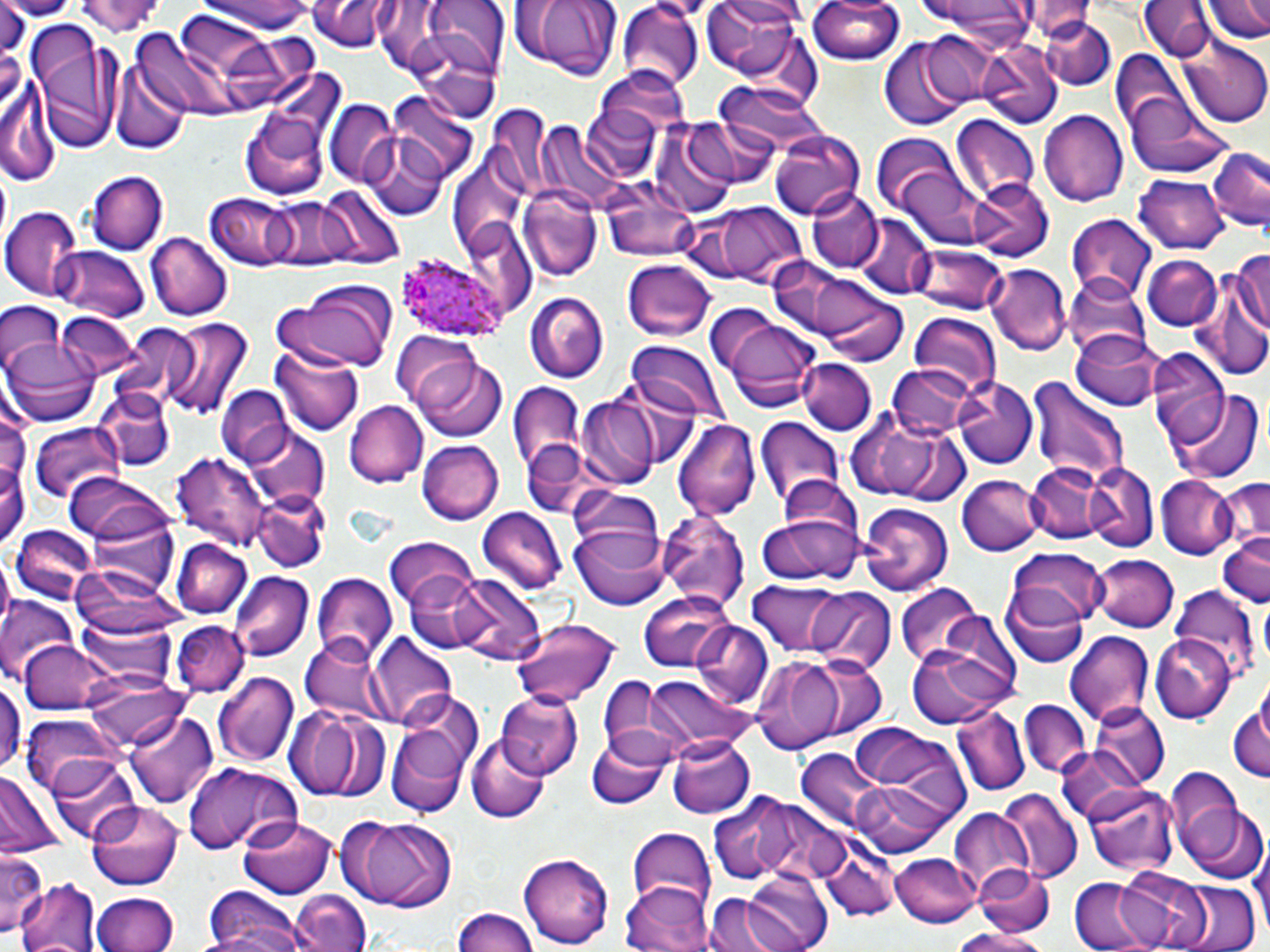 Approximate bounding boxes as named x1/y1/x2/y2 corners in pixels. Plasmodium ovale-infected red blood cell locations: (x1=397, y1=255, x2=504, y2=344). Uninfected red blood cell locations: (x1=76, y1=0, x2=167, y2=42), (x1=193, y1=0, x2=316, y2=35), (x1=310, y1=0, x2=395, y2=52), (x1=424, y1=0, x2=509, y2=77), (x1=507, y1=0, x2=624, y2=81), (x1=700, y1=0, x2=807, y2=88), (x1=804, y1=0, x2=908, y2=67), (x1=922, y1=0, x2=1037, y2=42), (x1=1202, y1=0, x2=1270, y2=43), (x1=1140, y1=1, x2=1212, y2=62), (x1=1018, y1=2, x2=1099, y2=43), (x1=618, y1=3, x2=704, y2=90), (x1=1, y1=7, x2=35, y2=54), (x1=1039, y1=16, x2=1115, y2=90), (x1=25, y1=21, x2=120, y2=151), (x1=403, y1=24, x2=504, y2=125), (x1=910, y1=29, x2=1002, y2=110), (x1=134, y1=31, x2=234, y2=117), (x1=220, y1=34, x2=332, y2=111), (x1=1180, y1=38, x2=1269, y2=127), (x1=879, y1=39, x2=974, y2=131), (x1=981, y1=42, x2=1061, y2=128), (x1=1110, y1=50, x2=1185, y2=132), (x1=109, y1=61, x2=188, y2=153), (x1=596, y1=67, x2=692, y2=144), (x1=715, y1=81, x2=828, y2=155), (x1=2, y1=87, x2=56, y2=187), (x1=238, y1=91, x2=335, y2=205), (x1=390, y1=94, x2=480, y2=184), (x1=1126, y1=94, x2=1235, y2=178), (x1=489, y1=96, x2=566, y2=197), (x1=325, y1=100, x2=398, y2=185), (x1=1039, y1=109, x2=1129, y2=207), (x1=680, y1=116, x2=793, y2=187), (x1=950, y1=116, x2=1038, y2=203), (x1=538, y1=124, x2=623, y2=211), (x1=649, y1=126, x2=738, y2=216), (x1=770, y1=130, x2=864, y2=218), (x1=361, y1=135, x2=450, y2=220), (x1=869, y1=135, x2=961, y2=212), (x1=1206, y1=145, x2=1269, y2=233), (x1=446, y1=150, x2=531, y2=254), (x1=886, y1=163, x2=992, y2=246), (x1=87, y1=171, x2=167, y2=255), (x1=1134, y1=172, x2=1227, y2=255), (x1=968, y1=178, x2=1052, y2=262), (x1=518, y1=187, x2=603, y2=283), (x1=314, y1=188, x2=404, y2=271), (x1=808, y1=189, x2=883, y2=274), (x1=208, y1=192, x2=303, y2=269), (x1=605, y1=192, x2=701, y2=263), (x1=266, y1=199, x2=347, y2=269), (x1=681, y1=201, x2=808, y2=287), (x1=1, y1=208, x2=83, y2=299), (x1=1066, y1=213, x2=1158, y2=303), (x1=855, y1=218, x2=936, y2=298), (x1=146, y1=230, x2=230, y2=319), (x1=910, y1=243, x2=1008, y2=315), (x1=1230, y1=244, x2=1270, y2=343), (x1=51, y1=245, x2=148, y2=323), (x1=1143, y1=255, x2=1222, y2=332), (x1=620, y1=259, x2=717, y2=341), (x1=770, y1=260, x2=890, y2=348), (x1=985, y1=264, x2=1071, y2=355), (x1=1190, y1=269, x2=1270, y2=384), (x1=1065, y1=280, x2=1147, y2=365), (x1=274, y1=287, x2=395, y2=372), (x1=818, y1=288, x2=908, y2=367), (x1=525, y1=291, x2=609, y2=384), (x1=0, y1=299, x2=65, y2=373), (x1=56, y1=312, x2=137, y2=380), (x1=907, y1=312, x2=1001, y2=394), (x1=716, y1=316, x2=822, y2=411), (x1=160, y1=318, x2=252, y2=422), (x1=116, y1=322, x2=209, y2=409), (x1=1072, y1=328, x2=1163, y2=410), (x1=393, y1=334, x2=483, y2=412), (x1=3, y1=339, x2=100, y2=427), (x1=629, y1=343, x2=722, y2=421), (x1=1148, y1=344, x2=1229, y2=446), (x1=270, y1=346, x2=367, y2=436), (x1=416, y1=357, x2=507, y2=443), (x1=796, y1=358, x2=878, y2=436), (x1=888, y1=364, x2=973, y2=440), (x1=598, y1=375, x2=706, y2=469), (x1=1026, y1=376, x2=1130, y2=488), (x1=952, y1=377, x2=1036, y2=470), (x1=508, y1=382, x2=586, y2=479), (x1=94, y1=385, x2=174, y2=468), (x1=218, y1=385, x2=290, y2=467), (x1=1172, y1=390, x2=1262, y2=481), (x1=577, y1=397, x2=660, y2=487), (x1=343, y1=400, x2=428, y2=487), (x1=843, y1=411, x2=971, y2=504), (x1=676, y1=418, x2=762, y2=520), (x1=754, y1=418, x2=842, y2=509), (x1=26, y1=423, x2=130, y2=510), (x1=240, y1=426, x2=331, y2=510), (x1=419, y1=440, x2=502, y2=525), (x1=522, y1=443, x2=596, y2=519), (x1=172, y1=449, x2=271, y2=554), (x1=0, y1=453, x2=26, y2=554), (x1=1084, y1=462, x2=1158, y2=551), (x1=1026, y1=463, x2=1104, y2=543), (x1=64, y1=473, x2=169, y2=545), (x1=1157, y1=474, x2=1239, y2=559), (x1=772, y1=475, x2=863, y2=558), (x1=958, y1=475, x2=1042, y2=557), (x1=1213, y1=475, x2=1269, y2=555), (x1=567, y1=489, x2=666, y2=577), (x1=252, y1=490, x2=330, y2=573), (x1=656, y1=503, x2=751, y2=616), (x1=859, y1=503, x2=955, y2=596), (x1=474, y1=507, x2=565, y2=592), (x1=87, y1=508, x2=180, y2=596), (x1=758, y1=510, x2=862, y2=587), (x1=11, y1=525, x2=97, y2=604), (x1=572, y1=528, x2=671, y2=612), (x1=1216, y1=532, x2=1268, y2=609), (x1=170, y1=539, x2=254, y2=620), (x1=387, y1=539, x2=480, y2=615), (x1=1008, y1=549, x2=1106, y2=631), (x1=1092, y1=553, x2=1179, y2=631), (x1=70, y1=569, x2=204, y2=644), (x1=230, y1=572, x2=313, y2=659), (x1=311, y1=572, x2=396, y2=661), (x1=410, y1=573, x2=544, y2=662), (x1=743, y1=579, x2=877, y2=663), (x1=895, y1=581, x2=993, y2=670), (x1=1000, y1=586, x2=1090, y2=670), (x1=803, y1=587, x2=896, y2=673), (x1=1170, y1=587, x2=1259, y2=677), (x1=639, y1=591, x2=736, y2=672), (x1=0, y1=600, x2=81, y2=687), (x1=78, y1=613, x2=176, y2=691), (x1=508, y1=617, x2=621, y2=709), (x1=172, y1=621, x2=249, y2=698), (x1=691, y1=621, x2=774, y2=709), (x1=1063, y1=629, x2=1155, y2=725), (x1=367, y1=631, x2=456, y2=727), (x1=1153, y1=632, x2=1234, y2=721), (x1=300, y1=635, x2=391, y2=725), (x1=19, y1=639, x2=117, y2=715), (x1=905, y1=641, x2=1009, y2=731), (x1=784, y1=654, x2=887, y2=741), (x1=749, y1=655, x2=850, y2=752), (x1=214, y1=670, x2=299, y2=769), (x1=0, y1=673, x2=23, y2=779), (x1=594, y1=673, x2=682, y2=762), (x1=645, y1=674, x2=753, y2=755), (x1=84, y1=675, x2=190, y2=750), (x1=495, y1=690, x2=582, y2=778), (x1=392, y1=692, x2=484, y2=788), (x1=1228, y1=697, x2=1270, y2=788), (x1=1018, y1=700, x2=1090, y2=781), (x1=286, y1=704, x2=386, y2=800), (x1=1091, y1=704, x2=1169, y2=786), (x1=950, y1=706, x2=1029, y2=798), (x1=125, y1=708, x2=217, y2=811), (x1=21, y1=716, x2=120, y2=798), (x1=846, y1=721, x2=972, y2=836), (x1=387, y1=727, x2=469, y2=818), (x1=585, y1=733, x2=671, y2=810), (x1=467, y1=736, x2=549, y2=823), (x1=666, y1=736, x2=753, y2=819), (x1=799, y1=743, x2=914, y2=839), (x1=1055, y1=745, x2=1146, y2=826), (x1=46, y1=754, x2=142, y2=844), (x1=183, y1=763, x2=300, y2=857), (x1=1165, y1=766, x2=1242, y2=855), (x1=0, y1=770, x2=66, y2=858), (x1=850, y1=777, x2=954, y2=855), (x1=1084, y1=784, x2=1179, y2=876), (x1=998, y1=790, x2=1081, y2=884), (x1=708, y1=797, x2=810, y2=885), (x1=88, y1=802, x2=186, y2=890), (x1=1180, y1=804, x2=1266, y2=885), (x1=948, y1=809, x2=1034, y2=898), (x1=337, y1=815, x2=458, y2=911), (x1=234, y1=817, x2=340, y2=900), (x1=626, y1=828, x2=715, y2=907), (x1=810, y1=828, x2=897, y2=922), (x1=0, y1=850, x2=45, y2=936), (x1=520, y1=852, x2=611, y2=950), (x1=889, y1=853, x2=982, y2=928), (x1=973, y1=861, x2=1056, y2=938), (x1=1116, y1=867, x2=1212, y2=951), (x1=738, y1=868, x2=833, y2=952), (x1=1068, y1=875, x2=1156, y2=952), (x1=18, y1=877, x2=103, y2=952), (x1=621, y1=880, x2=712, y2=952), (x1=1172, y1=881, x2=1261, y2=952), (x1=203, y1=888, x2=311, y2=952), (x1=289, y1=890, x2=371, y2=952), (x1=92, y1=892, x2=179, y2=952), (x1=707, y1=893, x2=791, y2=952), (x1=449, y1=909, x2=538, y2=952), (x1=956, y1=929, x2=1053, y2=952). Slide-level diagnosis: Plasmodium ovale. Light microscopy. 1000x magnification. Image is 1270×952 pixels. Thin blood film. May-Grünwald-Giemsa-stained preparation. One field of a larger specimen.